Assess this cell for malaria.
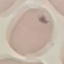

Uninfected.

Summary:
  - Capture: smartphone camera at the microscope eyepiece
  - Stain: Giemsa
  - Preparation: thin blood smear
  - Image type: cell patch, automatically extracted from a larger field of view and resized to 64 × 64 pixels